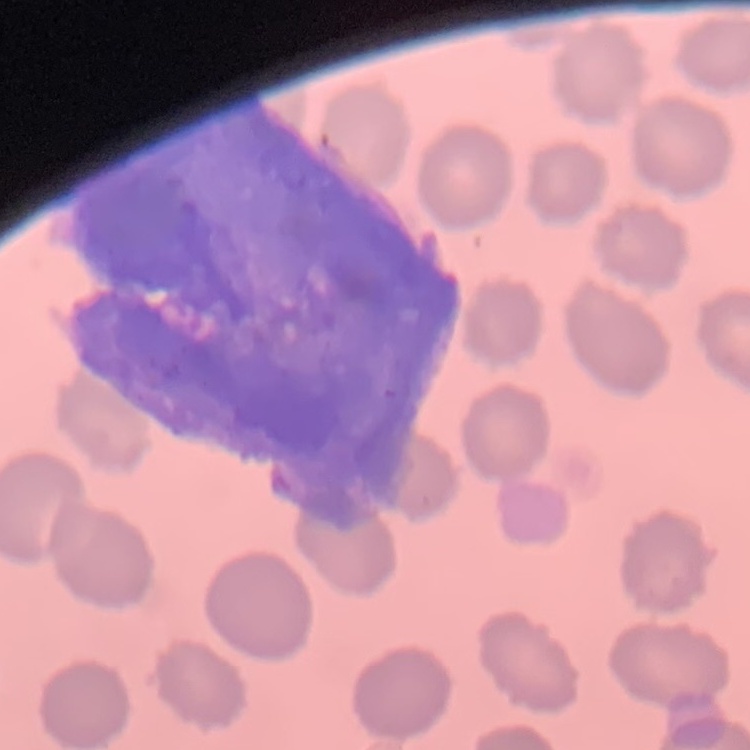 The red blood cells show no rouleaux formation. Field's or Giemsa stain. Thin blood film. Square crop of a larger photomicrograph.